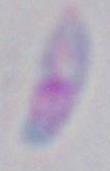
{
  "modality": "micrograph",
  "identification": "Toxoplasma gondii",
  "magnification": "1000x"
}